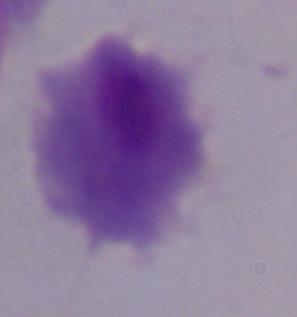

Summary:
  - Identification: trichomonad
  - Magnification: 1000x
  - Modality: micrograph